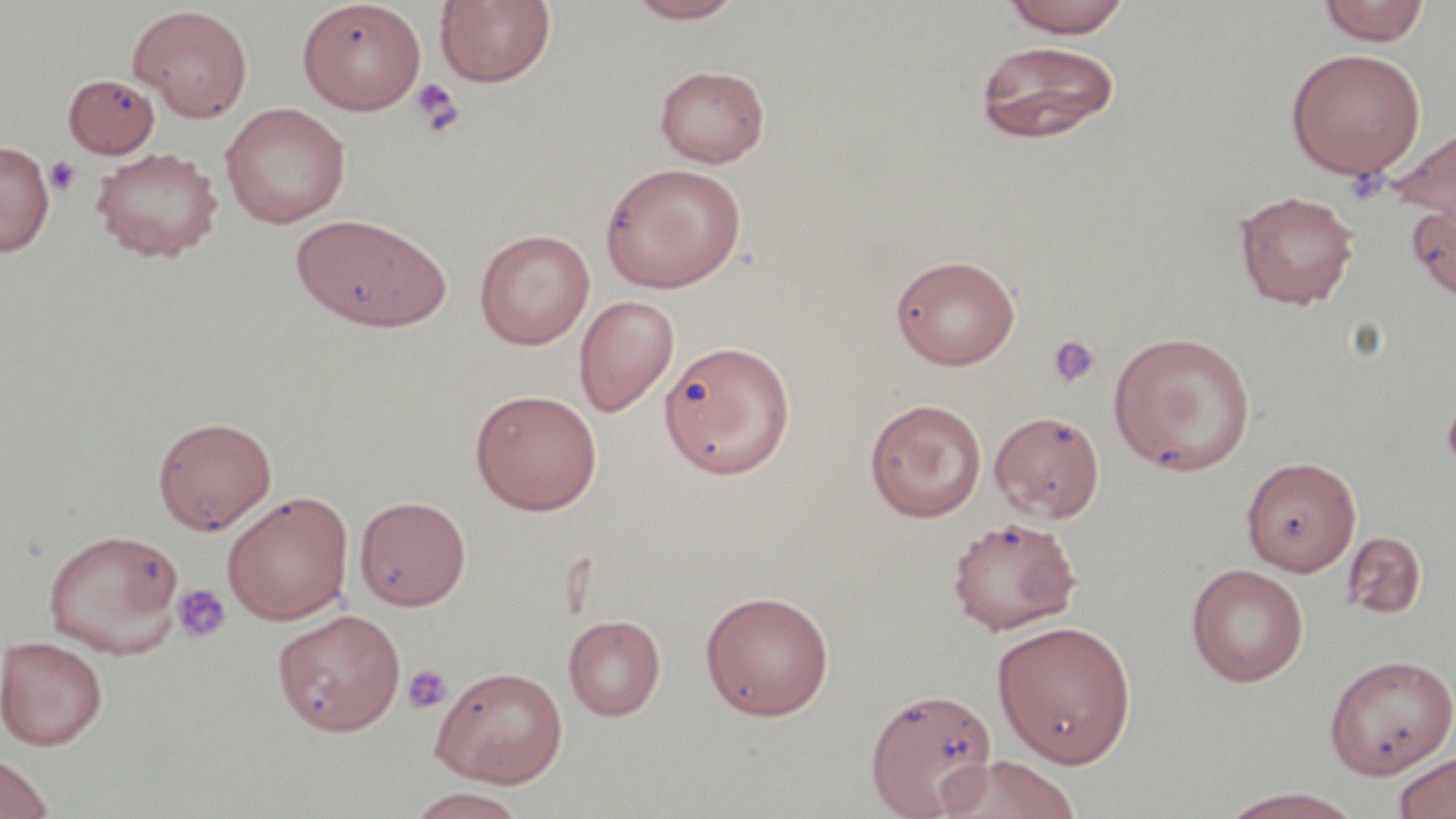 Approximate bounding boxes as [x1, y1, x2, y2] in pixels. Uninfected red blood cell locations: [297, 0, 426, 114], [435, 0, 556, 88], [625, 0, 745, 24], [1000, 0, 1133, 38], [1317, 1, 1430, 45], [128, 4, 253, 121], [974, 40, 1121, 143], [1285, 47, 1426, 179], [654, 64, 770, 167], [64, 73, 160, 158], [220, 103, 351, 228], [1388, 124, 1456, 239], [0, 140, 54, 256], [91, 146, 222, 263], [600, 161, 747, 292], [1235, 189, 1359, 309], [1406, 199, 1456, 301], [291, 213, 451, 332], [474, 228, 594, 350], [891, 254, 1021, 370], [574, 295, 679, 417], [1108, 330, 1256, 475], [659, 339, 795, 479], [470, 388, 603, 515], [864, 398, 987, 522], [989, 411, 1105, 522], [153, 416, 276, 534], [1241, 456, 1361, 575], [222, 490, 354, 624], [355, 495, 471, 611], [946, 516, 1082, 634], [43, 528, 184, 657], [1342, 531, 1426, 618], [1186, 563, 1309, 686], [699, 589, 835, 720], [272, 608, 405, 736], [563, 614, 665, 721], [992, 620, 1137, 767], [1, 635, 108, 750], [1324, 654, 1455, 778], [431, 666, 568, 787], [864, 686, 998, 816], [1392, 750, 1456, 819], [0, 752, 55, 819], [933, 755, 1082, 819], [1212, 787, 1369, 819], [403, 788, 528, 819]. Platelet locations: [409, 77, 464, 135], [45, 156, 80, 196], [1344, 166, 1389, 204], [1047, 334, 1102, 388], [1441, 396, 1456, 475], [172, 583, 230, 644], [403, 664, 453, 714]. Slide-level diagnosis: negative for blood parasites. Thin blood film. Single field of view. Image is 1456×819 pixels. 1000x magnification. May-Grünwald-Giemsa-stained preparation. Optical microscopy.